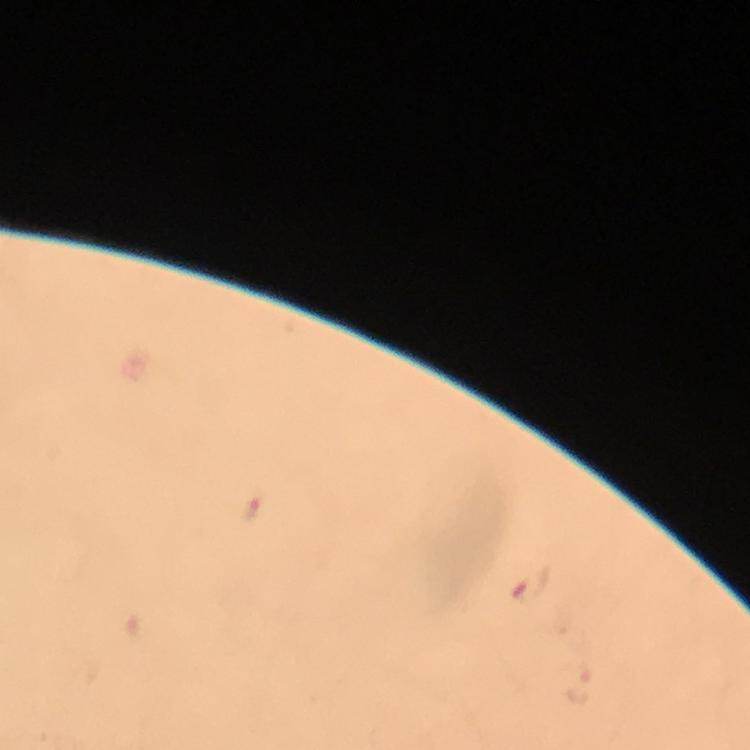
Approximate object centers, in pixels from the top-left corner.
Summary:
  - Plasmodium parasite locations: (x=253, y=508), (x=529, y=586)
  - Cropped from: a single field of view
  - Capture: smartphone mounted on the microscope
  - Immersion oil: applied
  - Magnification: 100x
  - Stain: Giemsa
  - Image size: 750×750 pixels
  - Context: from a malaria diagnostic workup
  - Preparation: thick blood smear